Identify the blood parasite species.
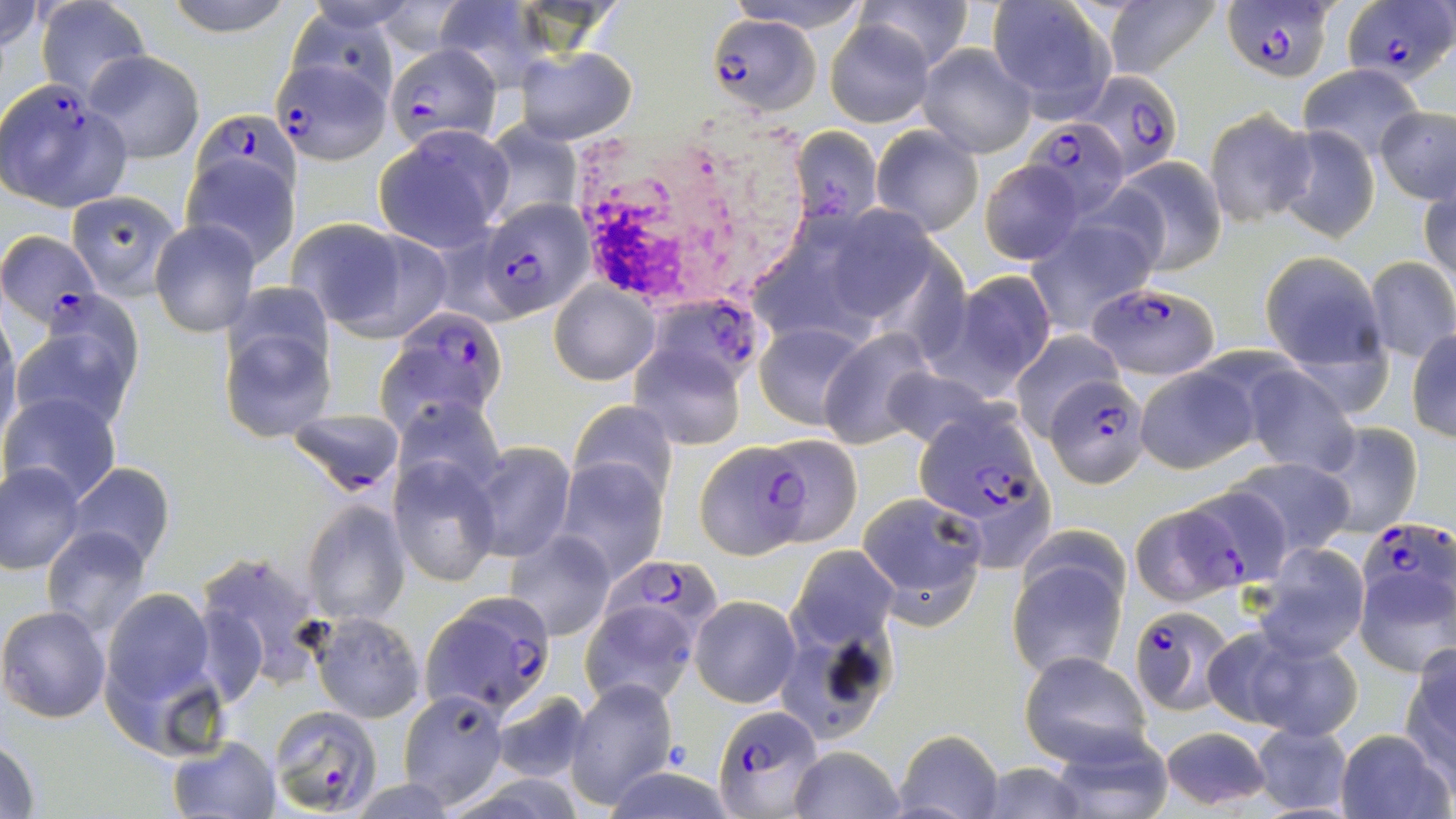
Plasmodium falciparum.

Summary:
  - Coordinate format: approximate bounding boxes as (x1, y1, x2, y2) in pixels
  - Uninfected red blood cell locations: (0, 0, 47, 54), (162, 0, 298, 37), (723, 0, 870, 32), (857, 0, 975, 73), (1102, 0, 1222, 79), (36, 1, 152, 102), (433, 2, 546, 89), (986, 2, 1115, 114), (824, 19, 935, 128), (918, 44, 1038, 158), (514, 45, 637, 143), (82, 51, 205, 162), (1299, 65, 1426, 162), (1204, 107, 1317, 230), (1374, 107, 1455, 204), (478, 121, 581, 228), (870, 124, 984, 236), (1276, 125, 1380, 242), (373, 126, 512, 250), (788, 127, 883, 226), (182, 155, 299, 267), (1108, 156, 1228, 274), (980, 161, 1083, 265), (1420, 181, 1456, 294), (67, 191, 181, 297), (1025, 218, 1157, 335), (149, 219, 260, 337), (291, 220, 450, 339), (1259, 254, 1385, 374), (1363, 254, 1455, 362), (942, 270, 1058, 393), (551, 283, 658, 385), (13, 310, 140, 435), (221, 316, 336, 439), (0, 318, 22, 449), (754, 320, 872, 430), (818, 328, 937, 446), (1408, 330, 1456, 442), (1010, 331, 1121, 439), (629, 343, 746, 450), (1132, 363, 1257, 473), (882, 365, 999, 451), (1240, 365, 1361, 476), (3, 393, 123, 509), (394, 396, 503, 496), (568, 400, 680, 503), (285, 412, 406, 494), (1309, 420, 1422, 539), (756, 433, 863, 547), (470, 442, 575, 562), (1229, 455, 1355, 560), (389, 456, 499, 586), (556, 461, 666, 580), (2, 462, 86, 574), (64, 462, 175, 569), (1182, 484, 1294, 591), (856, 491, 986, 623), (302, 501, 410, 625), (40, 525, 153, 638), (505, 530, 616, 641), (1256, 543, 1370, 660), (787, 545, 900, 648), (1006, 551, 1129, 681), (198, 552, 329, 689), (1353, 566, 1456, 677), (100, 586, 220, 719), (690, 596, 800, 707), (580, 599, 701, 707), (0, 605, 110, 722), (310, 612, 424, 723), (773, 621, 902, 743), (1232, 631, 1364, 741), (1401, 648, 1456, 774), (1019, 650, 1153, 767), (566, 678, 676, 807), (398, 689, 510, 807), (490, 691, 592, 782), (1246, 721, 1356, 817), (1154, 725, 1276, 812), (892, 728, 1006, 819), (1039, 728, 1172, 817), (1334, 729, 1452, 819), (0, 735, 42, 819), (168, 735, 279, 818), (787, 747, 906, 819), (968, 761, 1095, 819)
  - Plasmodium falciparum-infected red blood cell locations: (1225, 0, 1337, 83), (1343, 0, 1452, 85), (705, 14, 821, 115), (389, 41, 504, 167), (274, 52, 387, 163), (1084, 71, 1181, 181), (1, 81, 131, 211), (192, 109, 301, 212), (1022, 115, 1129, 220), (478, 198, 596, 321), (1, 227, 98, 326), (1092, 281, 1218, 377), (650, 299, 765, 391), (381, 309, 511, 429), (1046, 377, 1150, 487), (913, 408, 1040, 520), (696, 440, 810, 557), (1129, 502, 1246, 608), (1357, 514, 1451, 607), (603, 551, 722, 642), (421, 591, 557, 717), (1126, 607, 1237, 715), (267, 705, 383, 816), (713, 706, 825, 816)
  - Image size: 1456×819 pixels
  - Field of view: single
  - Modality: light microscopy
  - Stain: May-Grünwald-Giemsa
  - Preparation: thin blood smear
  - Magnification: 1000x